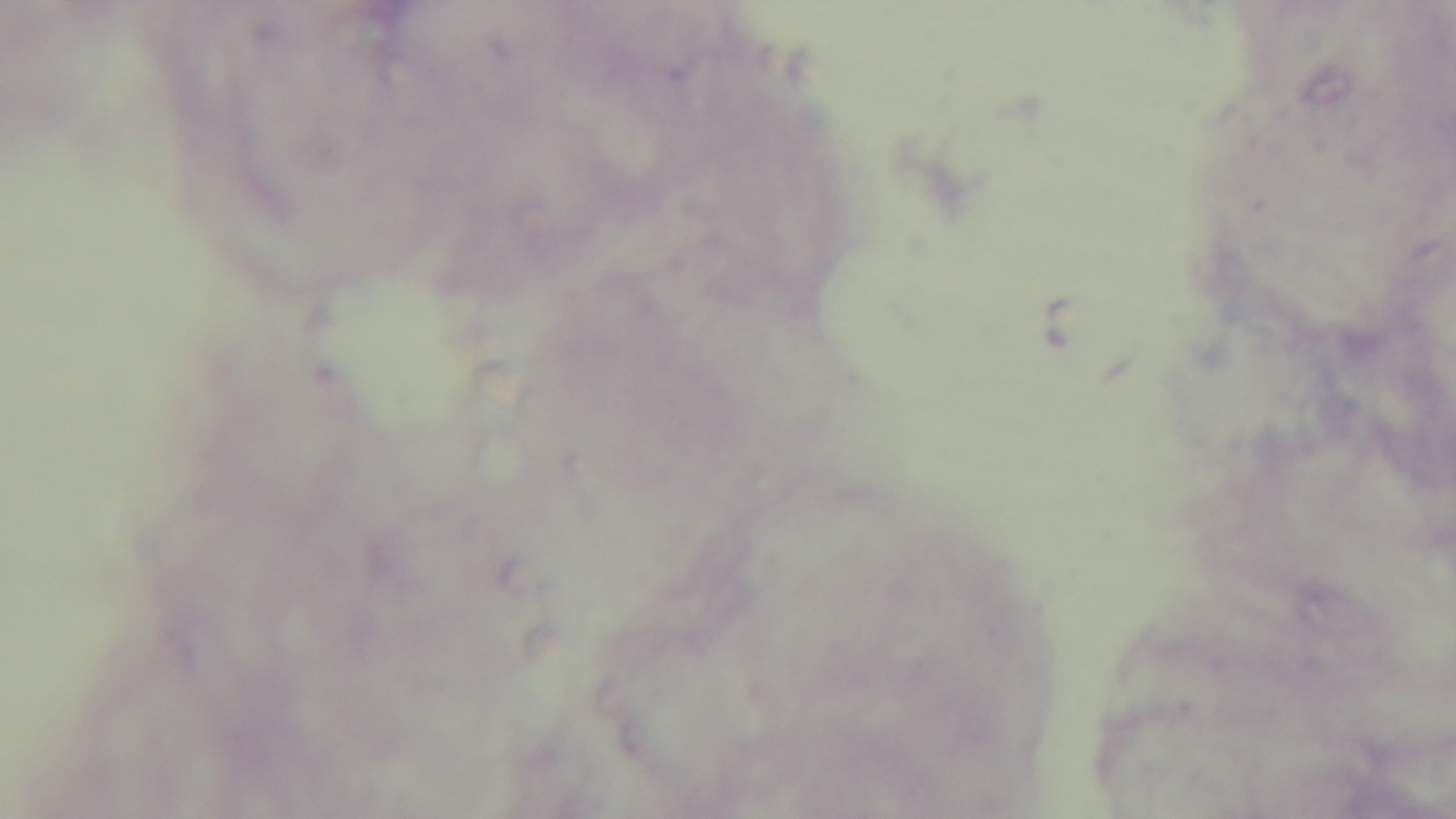
Malaria status: negative. Light microscopy. Single field of view. Giemsa-stained. Preparation: thick blood film. Mounted 4K digital camera. 100x oil-immersion objective.